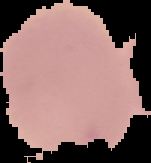

Summary:
  - Image size: 151×163 pixels
  - Malaria status: uninfected
  - Preparation: thin blood smear
  - Image type: cell region segmented out of the field of view; surrounding area masked to black